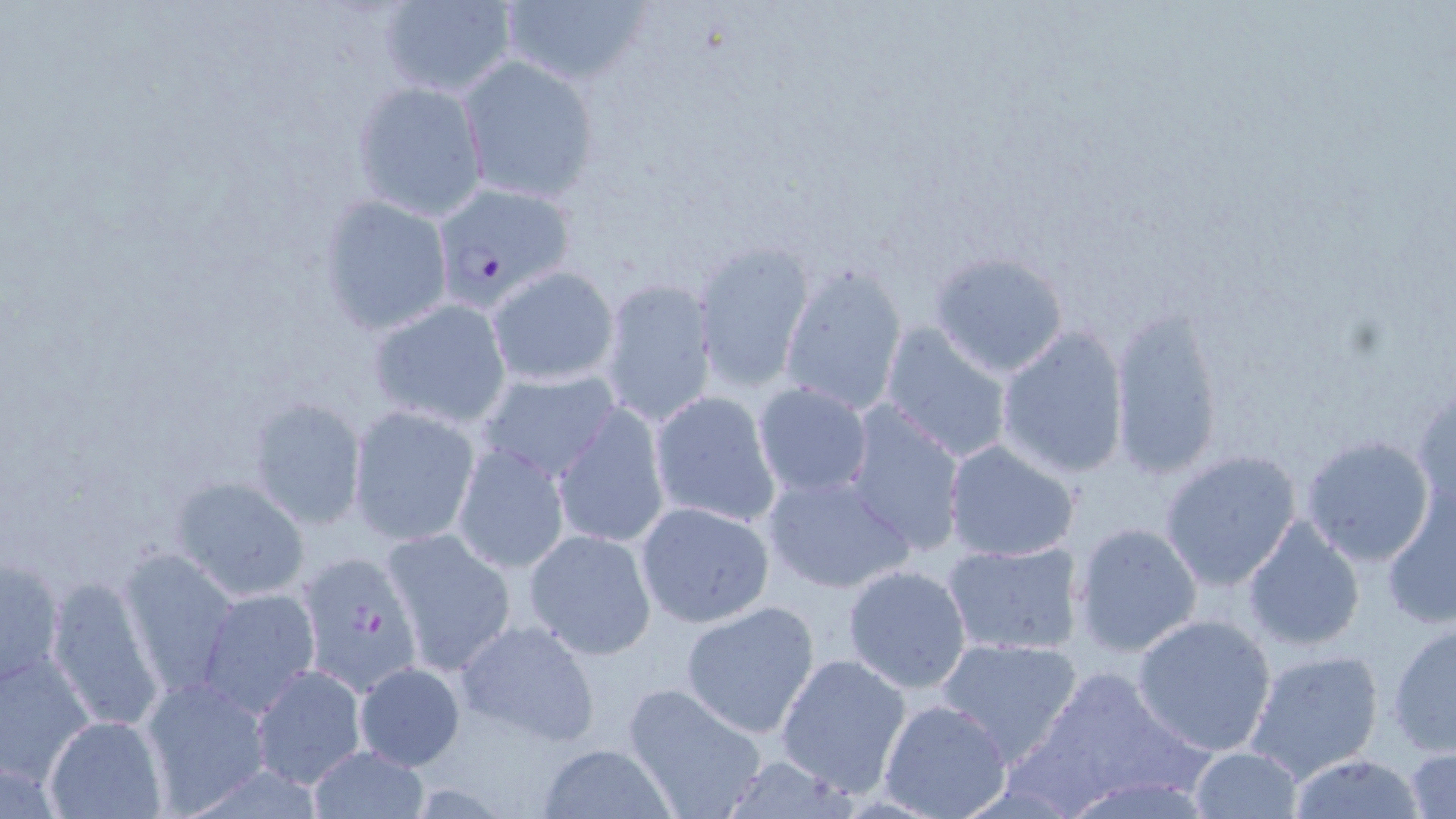

Approximate bounding boxes as named x1/y1/x2/y2 corners in pixels. Uninfected red blood cell locations: (x1=497, y1=0, x2=651, y2=88), (x1=376, y1=1, x2=518, y2=98), (x1=459, y1=56, x2=600, y2=203), (x1=351, y1=80, x2=488, y2=221), (x1=320, y1=196, x2=453, y2=335), (x1=694, y1=239, x2=813, y2=391), (x1=931, y1=252, x2=1068, y2=376), (x1=778, y1=262, x2=908, y2=416), (x1=487, y1=266, x2=619, y2=388), (x1=596, y1=277, x2=719, y2=430), (x1=367, y1=299, x2=511, y2=430), (x1=1109, y1=306, x2=1224, y2=481), (x1=880, y1=322, x2=1015, y2=465), (x1=996, y1=325, x2=1130, y2=480), (x1=476, y1=367, x2=623, y2=484), (x1=753, y1=382, x2=873, y2=498), (x1=1412, y1=384, x2=1456, y2=519), (x1=649, y1=390, x2=780, y2=531), (x1=249, y1=396, x2=367, y2=530), (x1=841, y1=401, x2=967, y2=556), (x1=554, y1=403, x2=669, y2=548), (x1=348, y1=407, x2=483, y2=546), (x1=1301, y1=435, x2=1436, y2=567), (x1=452, y1=441, x2=570, y2=574), (x1=943, y1=441, x2=1078, y2=563), (x1=1159, y1=450, x2=1303, y2=590), (x1=761, y1=468, x2=916, y2=596), (x1=174, y1=477, x2=311, y2=601), (x1=1380, y1=485, x2=1455, y2=633), (x1=634, y1=500, x2=776, y2=629), (x1=1241, y1=515, x2=1365, y2=651), (x1=1072, y1=522, x2=1202, y2=656), (x1=383, y1=527, x2=517, y2=676), (x1=521, y1=528, x2=656, y2=659), (x1=942, y1=540, x2=1079, y2=657), (x1=120, y1=549, x2=240, y2=694), (x1=1, y1=552, x2=66, y2=688), (x1=840, y1=564, x2=971, y2=693), (x1=46, y1=575, x2=165, y2=734), (x1=196, y1=588, x2=319, y2=715), (x1=680, y1=601, x2=821, y2=738), (x1=1131, y1=613, x2=1278, y2=756), (x1=455, y1=619, x2=600, y2=747), (x1=1386, y1=621, x2=1455, y2=757), (x1=933, y1=635, x2=1084, y2=766), (x1=1242, y1=646, x2=1386, y2=783), (x1=0, y1=649, x2=97, y2=787), (x1=774, y1=652, x2=913, y2=798), (x1=352, y1=661, x2=466, y2=771), (x1=250, y1=664, x2=364, y2=788), (x1=1014, y1=664, x2=1204, y2=811), (x1=139, y1=677, x2=271, y2=811), (x1=621, y1=680, x2=770, y2=819), (x1=878, y1=699, x2=1012, y2=819), (x1=43, y1=715, x2=166, y2=819), (x1=305, y1=744, x2=431, y2=819), (x1=534, y1=744, x2=674, y2=818), (x1=1405, y1=744, x2=1456, y2=818), (x1=1188, y1=746, x2=1304, y2=817), (x1=1286, y1=754, x2=1430, y2=817), (x1=713, y1=756, x2=867, y2=817). Plasmodium falciparum-infected red blood cell locations: (x1=435, y1=184, x2=581, y2=312), (x1=295, y1=551, x2=423, y2=694). Slide-level diagnosis: Plasmodium falciparum. Light microscopy. May-Grünwald-Giemsa-stained preparation. Image is 1456×819 pixels. Captured at 1000x magnification. One field of a larger specimen. Thin blood smear.